Give the position of every leukocyte visible.
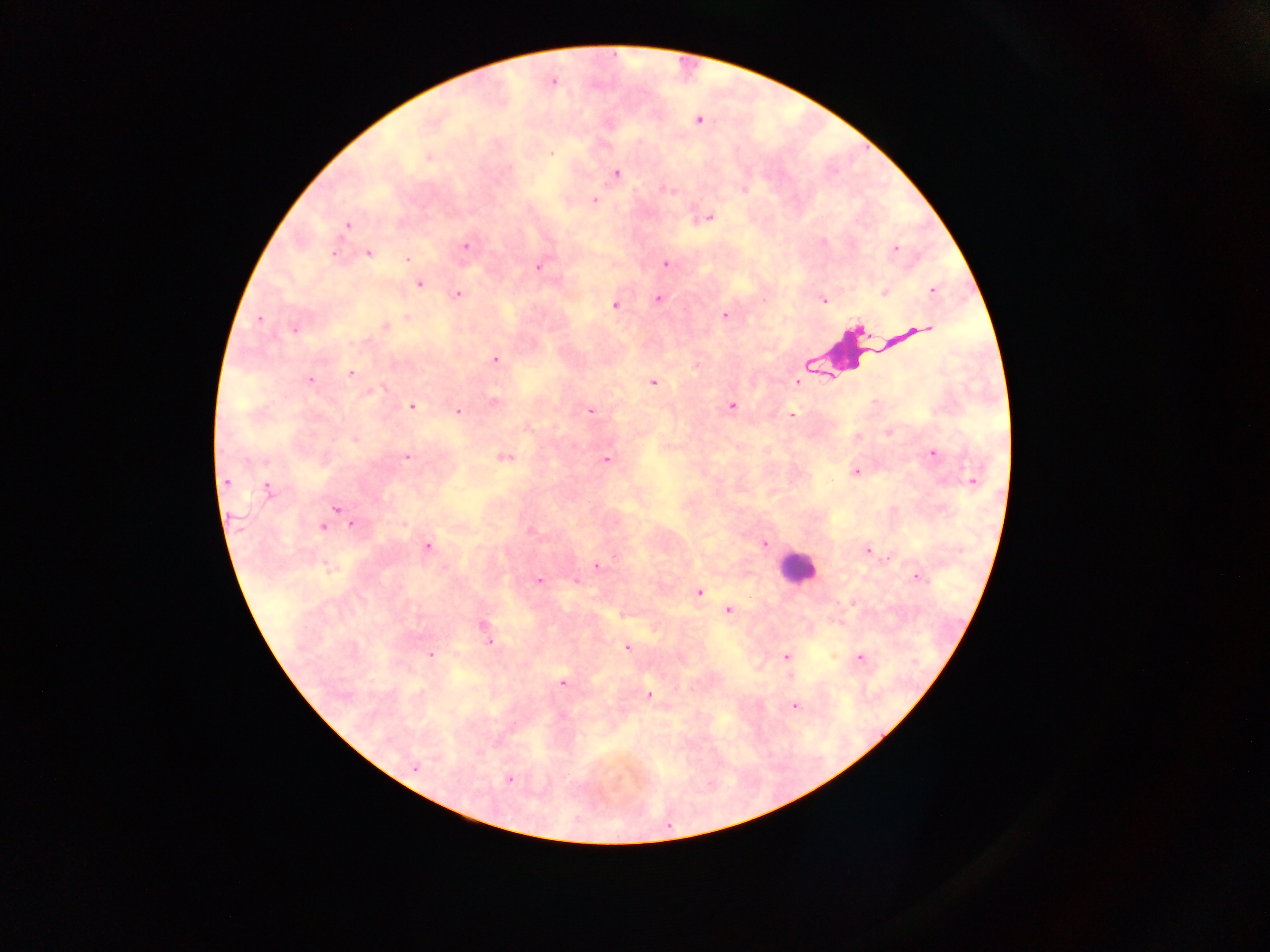
Approximate centers as {x, y} in pixels.
Leukocytes: {853, 354}, {796, 567}.

Summary:
  - Plasmodium parasite locations: {553, 82}, {698, 120}, {551, 154}, {428, 157}, {616, 173}, {668, 189}, {594, 200}, {709, 217}, {346, 225}, {465, 246}, {895, 248}, {368, 254}, {334, 255}, {407, 259}, {665, 263}, {538, 267}, {420, 284}, {932, 291}, {884, 292}, {459, 294}, {658, 300}, {824, 301}, {615, 305}, {724, 316}, {407, 318}, {260, 319}, {385, 325}, {928, 328}, {295, 330}, {496, 360}, {696, 366}, {351, 374}, {310, 380}, {797, 382}, {653, 383}, {493, 402}, {731, 405}, {411, 406}, {590, 410}, {459, 412}, {792, 414}, {888, 432}, {354, 440}, {933, 453}, {407, 457}, {503, 458}, {606, 459}, {856, 472}, {972, 480}, {227, 483}, {269, 489}, {336, 509}, {352, 525}, {322, 527}, {531, 531}, {765, 544}, {427, 546}, {867, 550}, {615, 558}, {597, 566}, {918, 577}, {539, 580}, {576, 581}, {700, 592}, {853, 602}, {728, 610}, {482, 624}, {489, 642}, {626, 648}, {430, 656}, {786, 657}, {860, 657}, {790, 676}, {562, 682}, {649, 695}, {795, 706}, {415, 767}, {510, 779}
  - Preparation: thick blood film
  - Country: Ghana
  - Image size: 1270×952 pixels
  - Field of view: single
  - Capture: mobile-phone photograph through a microscope